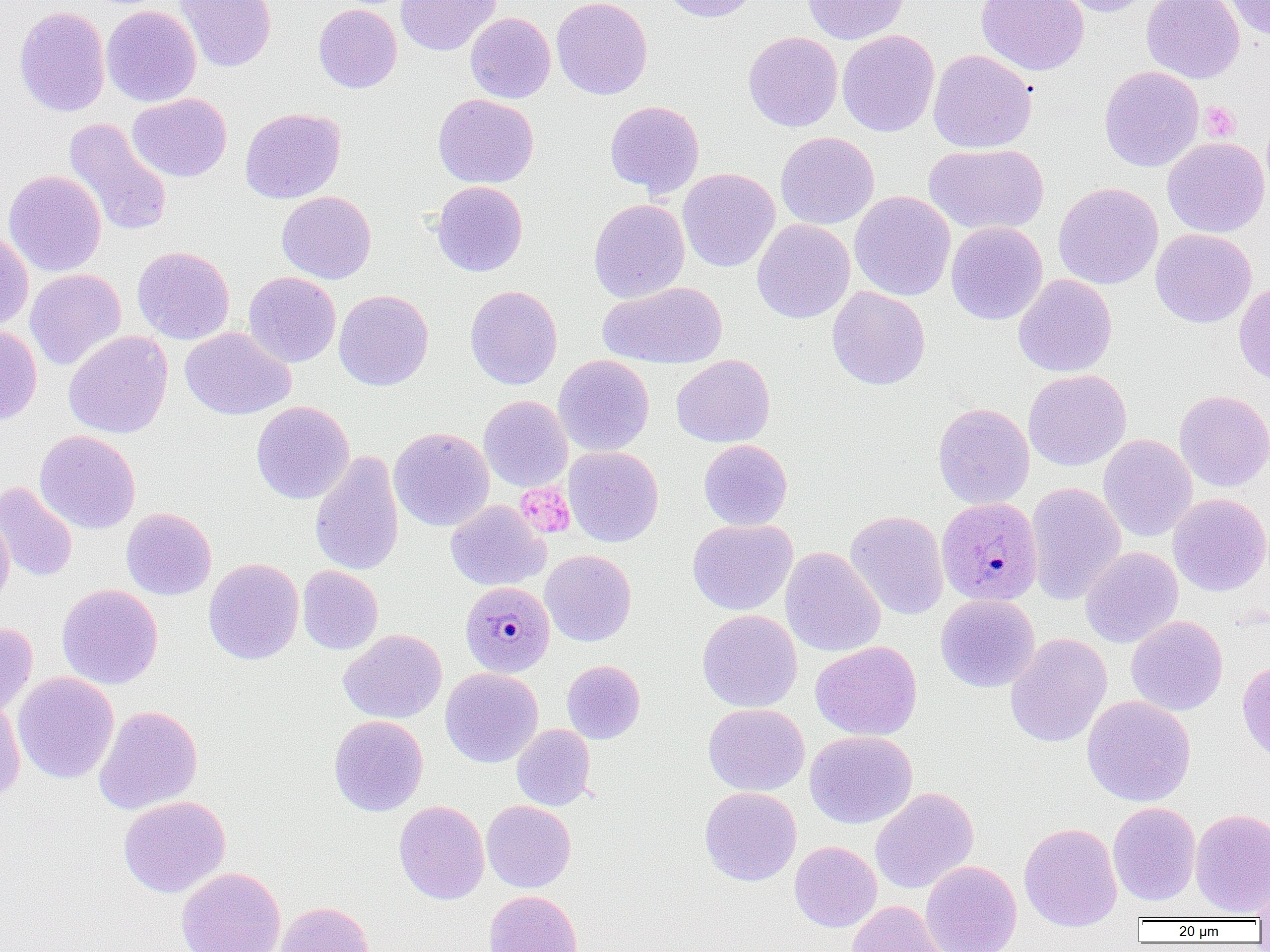
Summary:
  - Coordinate format: approximate bounding boxes as (x1, y1, x2, y2) in pixels
  - Platelet locations: (1201, 101, 1240, 141), (515, 482, 575, 538)
  - Uninfected red blood cell locations: (174, 0, 277, 72), (395, 0, 502, 56), (551, 0, 653, 100), (660, 0, 762, 22), (802, 0, 908, 44), (976, 0, 1089, 75), (1053, 0, 1158, 16), (1141, 0, 1244, 83), (1224, 0, 1270, 41), (313, 3, 402, 93), (14, 6, 110, 117), (101, 6, 201, 107), (465, 12, 555, 103), (837, 29, 939, 137), (743, 31, 843, 132), (928, 49, 1037, 153), (1099, 66, 1204, 172), (127, 93, 232, 182), (433, 93, 539, 188), (604, 101, 704, 197), (240, 107, 346, 204), (64, 118, 172, 237), (775, 131, 879, 230), (1163, 137, 1269, 238), (924, 143, 1049, 235), (678, 168, 779, 272), (4, 170, 106, 277), (432, 181, 528, 276), (1053, 183, 1163, 289), (276, 191, 376, 284), (849, 191, 955, 301), (589, 199, 690, 303), (752, 219, 855, 324), (946, 222, 1047, 325), (1150, 228, 1257, 328), (0, 230, 34, 332), (132, 246, 235, 344), (24, 268, 126, 370), (243, 272, 341, 368), (1013, 273, 1118, 377), (1234, 280, 1270, 385), (599, 281, 727, 368), (465, 285, 563, 390), (827, 286, 930, 390), (333, 289, 434, 391), (0, 325, 42, 425), (180, 327, 295, 420), (64, 330, 173, 439), (671, 354, 775, 447), (553, 355, 654, 456), (1023, 369, 1131, 471), (1174, 390, 1270, 492), (479, 395, 573, 492), (251, 401, 354, 504), (933, 403, 1034, 509), (388, 427, 494, 531), (34, 430, 141, 534), (1098, 434, 1197, 542), (699, 439, 793, 531), (564, 446, 663, 547), (310, 451, 405, 576), (0, 481, 78, 582), (1025, 481, 1126, 605), (1168, 493, 1270, 596), (446, 500, 550, 591), (121, 507, 216, 600), (0, 508, 14, 609), (845, 510, 948, 620), (687, 518, 798, 615), (1080, 546, 1183, 647), (780, 547, 885, 657), (540, 549, 636, 647), (203, 558, 304, 664), (297, 565, 383, 654), (57, 584, 163, 689), (935, 594, 1040, 692), (697, 609, 802, 712), (1126, 616, 1228, 716), (0, 622, 38, 723), (338, 629, 447, 723), (1005, 633, 1112, 748), (811, 641, 922, 741), (1237, 657, 1270, 764), (562, 660, 645, 744), (440, 668, 543, 768), (12, 672, 119, 783), (1082, 696, 1196, 806), (0, 698, 25, 802), (703, 703, 810, 796), (93, 705, 204, 814), (328, 715, 428, 816), (512, 724, 595, 811), (805, 731, 917, 828), (699, 787, 801, 886), (870, 787, 979, 895), (118, 795, 231, 898), (394, 800, 489, 904), (481, 800, 576, 893), (1108, 802, 1201, 906), (1190, 808, 1270, 917), (1019, 822, 1122, 931), (789, 841, 881, 932), (921, 860, 1022, 952), (176, 867, 286, 952), (1251, 879, 1270, 927), (483, 890, 583, 952), (274, 901, 375, 952), (847, 901, 949, 952)
  - Plasmodium malariae-infected red blood cell locations: (936, 498, 1043, 606), (460, 581, 555, 677)
  - Slide-level diagnosis: Plasmodium malariae
  - Magnification: 1000x
  - Modality: optical microscopy
  - Preparation: thin blood film
  - Image size: 1270×952 pixels
  - Field of view: single